Assess this cell for malaria.
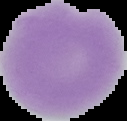

Uninfected.

From a thin blood film. Image is 127×121 pixels. Segmented cell region on a black background.